Report the malaria status of this cell.
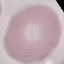
Uninfected.

image_type: automatically extracted cell patch, resized to 64 × 64 pixels
stain: Giemsa
capture: smartphone through the microscope eyepiece
preparation: thin blood smear